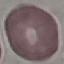

result = no malaria parasites detected
preparation = thin blood smear
image type = cell patch, automatically extracted from a larger field of view and resized to 64 × 64 pixels
stain = Giemsa
capture = smartphone through the microscope eyepiece